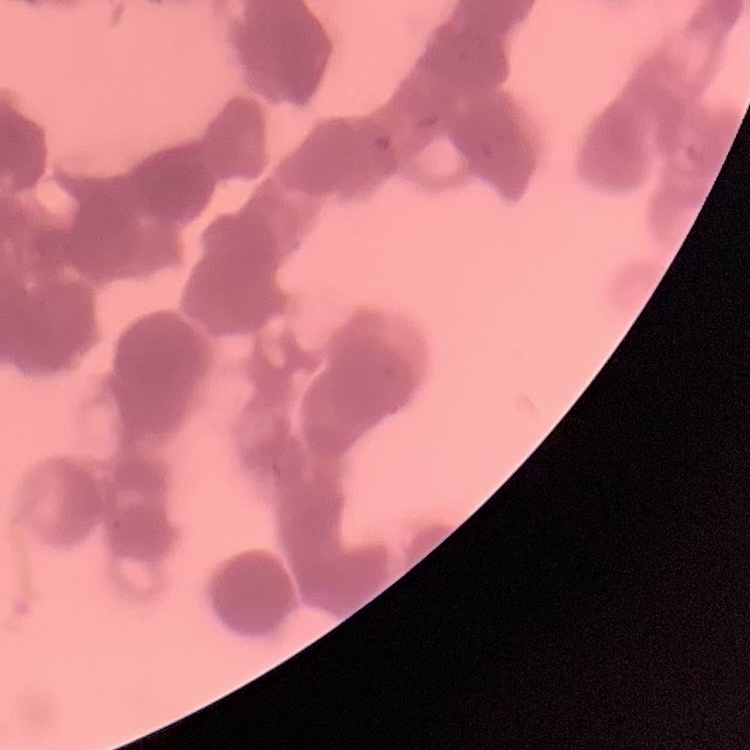

red blood cell morphology = rouleaux formation
stain = Field's or Giemsa
preparation = thin blood smear
image type = one tile cut from a larger photomicrograph